Describe the morphology of the red blood cells.
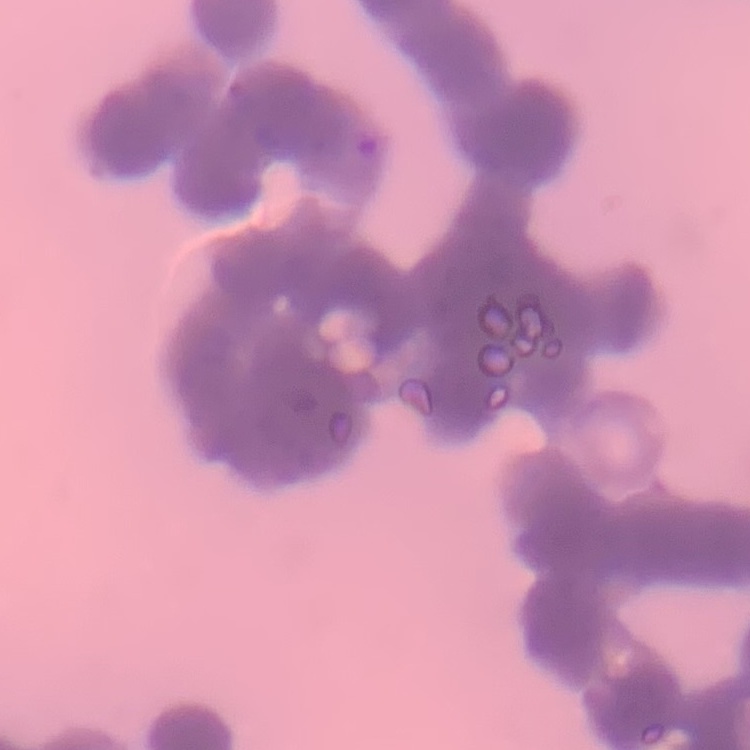
Rouleaux formation.

Thin blood smear. Field's or Giemsa stain. Square crop of a larger photomicrograph.